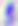
modality = micrograph
magnification = 400x
identification = Toxoplasma gondii